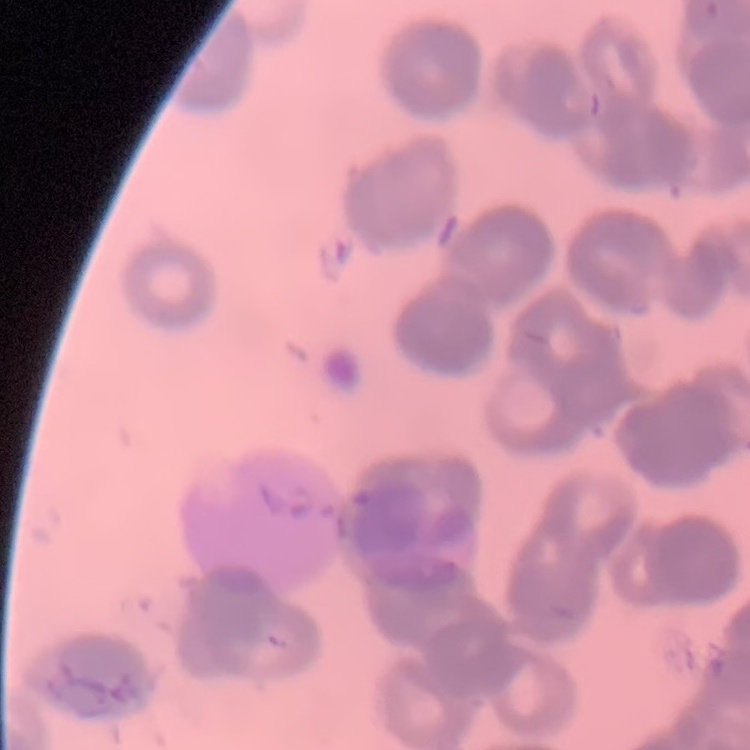

Summary:
  - Erythrocyte morphology: rouleaux formation
  - Preparation: thin peripheral smear
  - Stain: Field's or Giemsa
  - Image type: one tile cut from a larger photomicrograph